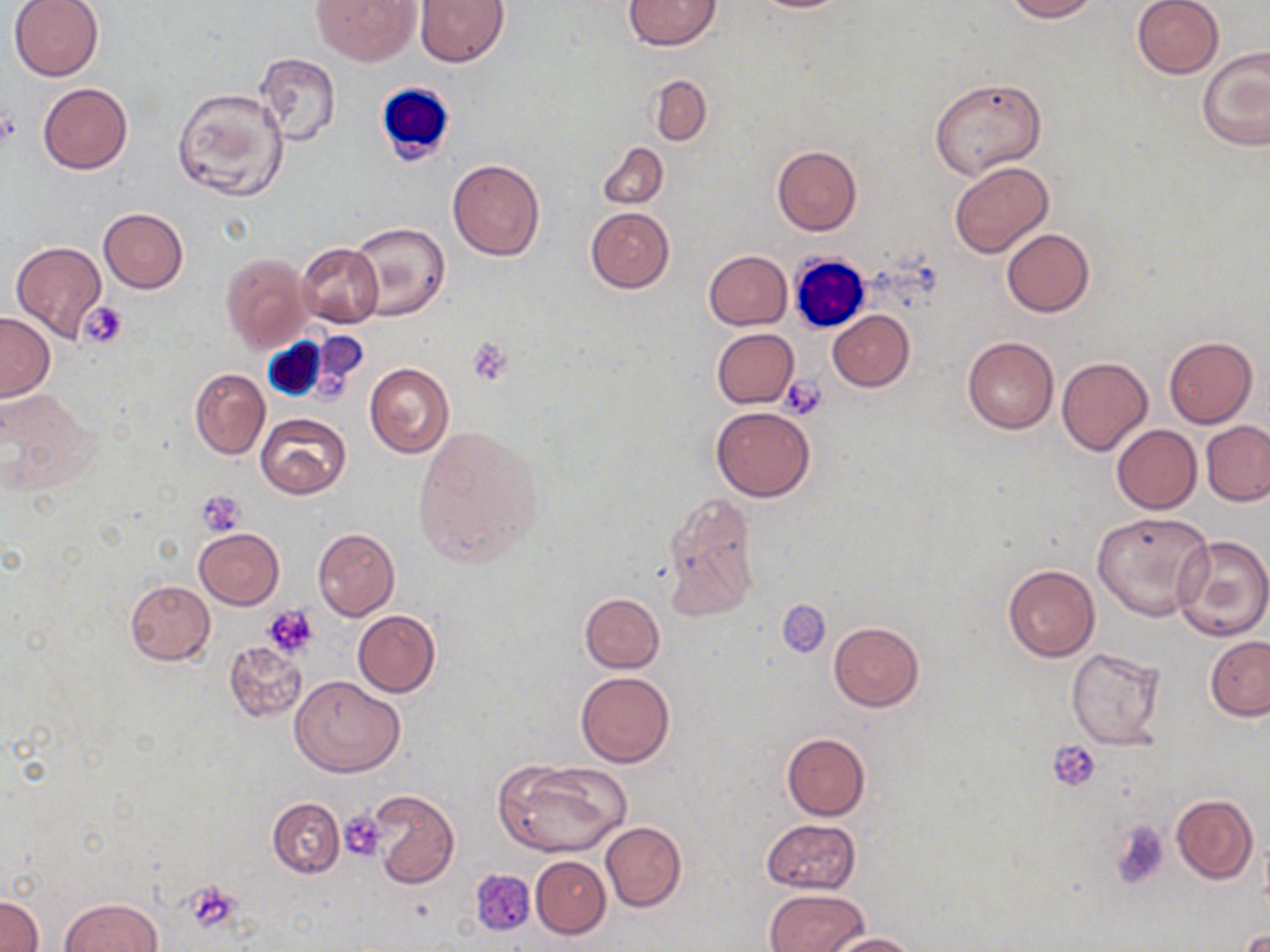
Summary:
  - Coordinate format: approximate bounding boxes as (x1,y1)-(x2,y2) corner pairs in pixels
  - Uninfected red blood cell locations: (8,0)-(105,81), (313,0)-(419,66), (414,0)-(510,67), (623,0)-(721,50), (744,0)-(853,13), (1004,0)-(1097,21), (1132,0)-(1223,78), (1197,48)-(1270,151), (255,52)-(341,144), (649,74)-(712,146), (930,78)-(1046,179), (39,82)-(132,174), (172,87)-(289,200), (596,141)-(668,210), (772,145)-(861,235), (447,159)-(545,261), (949,161)-(1054,259), (585,207)-(675,293), (98,208)-(189,294), (348,222)-(449,321), (1002,229)-(1094,317), (10,241)-(107,342), (295,242)-(384,328), (703,250)-(792,330), (220,253)-(311,352), (828,310)-(913,390), (0,312)-(54,400), (711,328)-(799,407), (1164,336)-(1257,428), (963,337)-(1059,434), (1056,357)-(1152,455), (364,363)-(454,457), (189,368)-(270,460), (0,389)-(98,495), (710,407)-(816,502), (255,412)-(352,499), (1201,421)-(1270,505), (411,423)-(546,570), (1111,424)-(1202,514), (661,491)-(763,624), (1091,511)-(1214,622), (313,527)-(399,620), (195,528)-(285,609), (1172,534)-(1270,642), (1003,564)-(1099,662), (124,580)-(215,664), (579,592)-(664,672), (778,599)-(832,658), (353,609)-(439,698), (829,621)-(923,710), (1205,634)-(1270,720), (223,640)-(307,722), (1066,646)-(1168,750), (576,671)-(675,767), (290,675)-(405,777), (780,732)-(869,820), (496,759)-(631,858), (367,789)-(459,889), (1171,794)-(1257,883), (267,797)-(344,878), (761,818)-(861,893), (600,821)-(686,912), (531,856)-(610,939), (765,888)-(868,952), (0,894)-(43,952), (58,898)-(161,952), (1236,927)-(1269,951), (823,931)-(919,951)
  - Platelet locations: (0,110)-(21,147), (80,303)-(128,350), (466,336)-(513,384), (782,376)-(827,418), (197,489)-(248,535), (262,604)-(319,659), (1049,740)-(1101,791), (339,810)-(389,863), (1110,821)-(1170,888), (184,881)-(242,932)
  - White blood cell locations: (375,83)-(456,167), (788,253)-(871,334), (257,331)-(347,401)
  - Slide-level diagnosis: negative for blood parasites
  - Image size: 1270×952 pixels
  - Stain: May-Grünwald-Giemsa
  - Preparation: thin blood smear
  - Magnification: 1000x
  - Field of view: single
  - Modality: optical microscopy